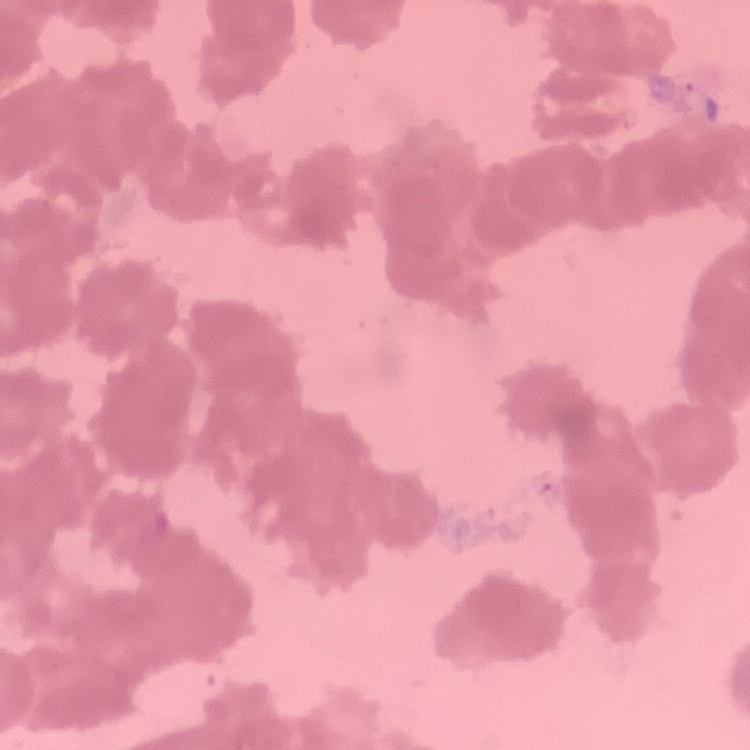
{
  "red_blood_cell_morphology": "rouleaux formation",
  "stain": "Field's or Giemsa",
  "image_type": "square crop of a larger photomicrograph",
  "preparation": "thin peripheral smear"
}